Describe the morphology of the red blood cells.
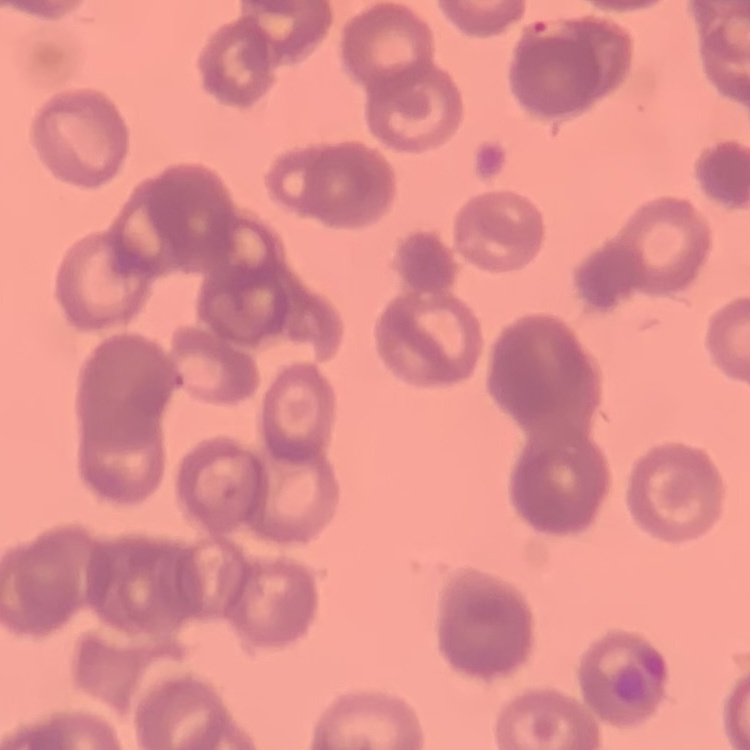

Rouleaux formation.

{
  "image_type": "square crop of a larger photomicrograph",
  "stain": "Field's or Giemsa",
  "preparation": "thin peripheral smear"
}